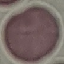

malaria status = uninfected
image type = automatically extracted cell patch, resized to 64 × 64 pixels
capture = smartphone camera at the microscope eyepiece
preparation = thin blood film
stain = Giemsa